Report the malaria status.
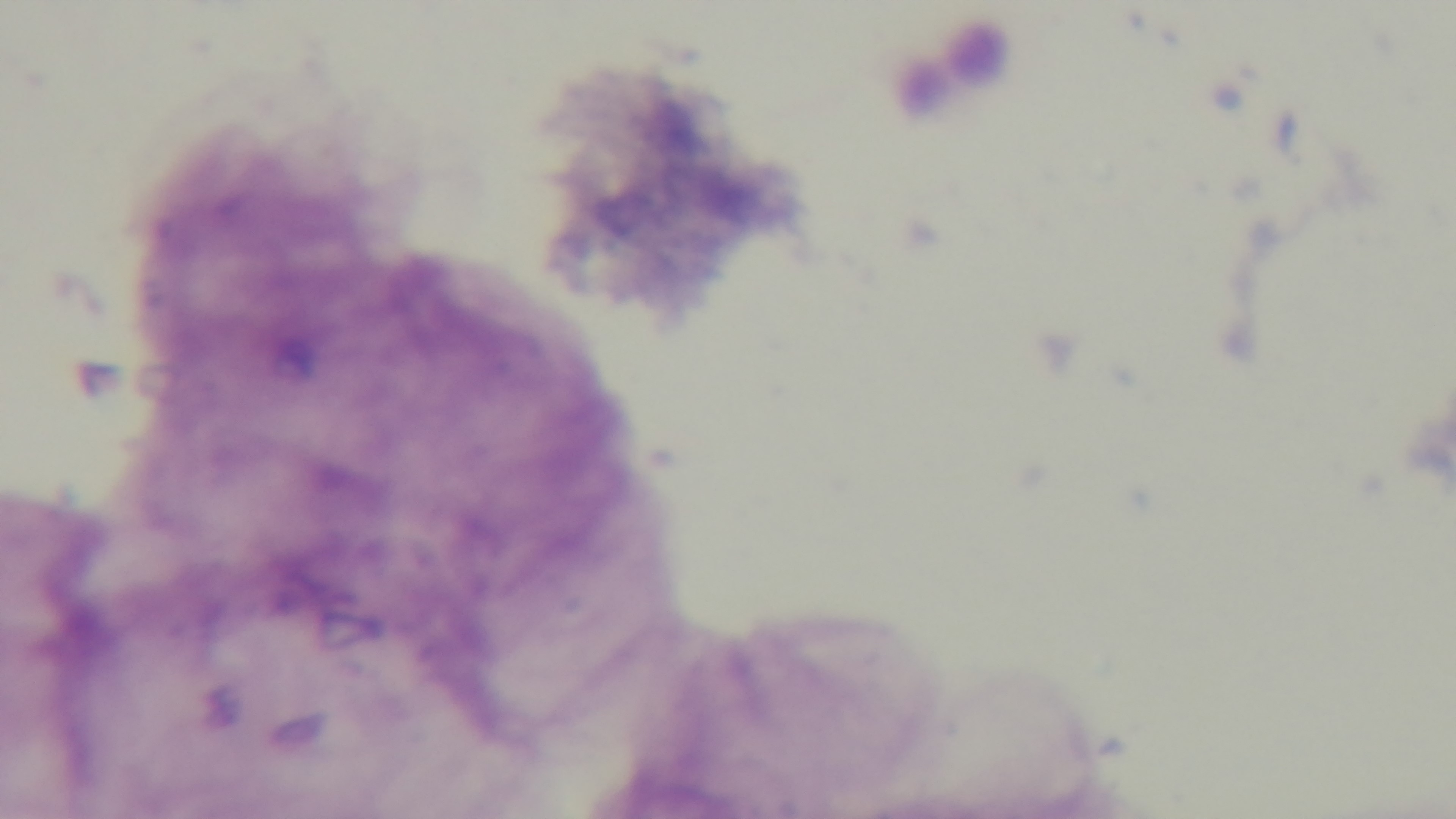
It is uninfected.

field_of_view: one from the slide
modality: light microscopy
preparation: thick smear
stain: Giemsa
capture: mounted 4K digital camera
objective: 100x oil immersion